Outline every artifact (platelet-like body, stain precipitate, or debris).
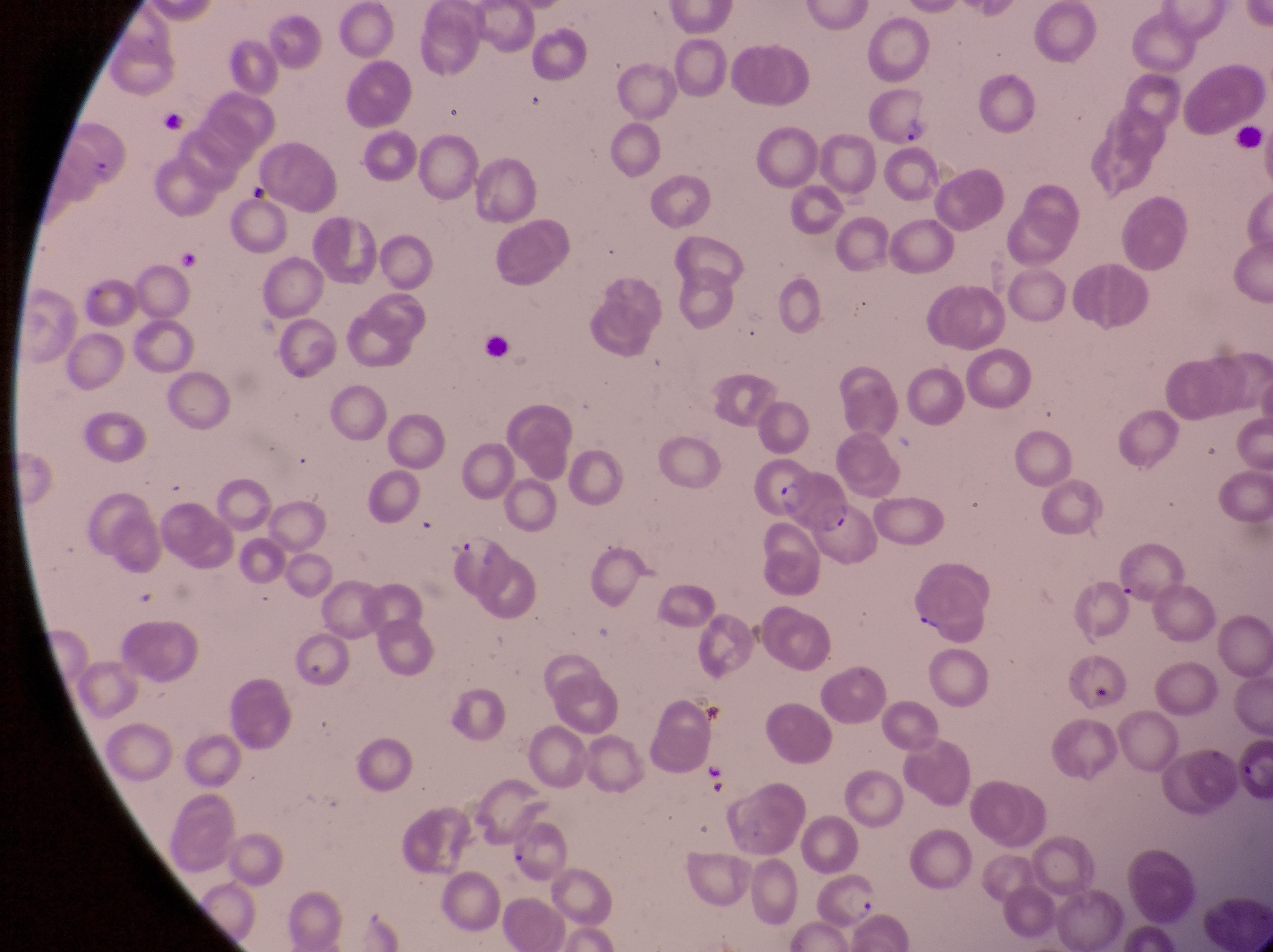

Approximate bounding boxes as {left, top, right, bottom} in pixels.
Artifacts (platelet-like body, stain precipitate, or debris): {155, 104, 197, 141}, {234, 178, 277, 210}, {175, 247, 198, 274}.

Parasitised red blood cell locations: {871, 77, 936, 149}, {70, 123, 133, 188}, {776, 472, 861, 539}, {811, 866, 885, 929}. Single field of view. Magnification of 1000x. Image is 1273×952 pixels. Collected in Uganda. Photographed through the eyepiece of an Olympus CX-23 microscope with a smartphone camera. Thin blood smear.